Classify this cell by malaria status.
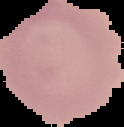

It is uninfected.

Summary:
  - Image type: segmented cell region with the area outside set to black
  - Preparation: thin blood film
  - Image size: 124×127 pixels